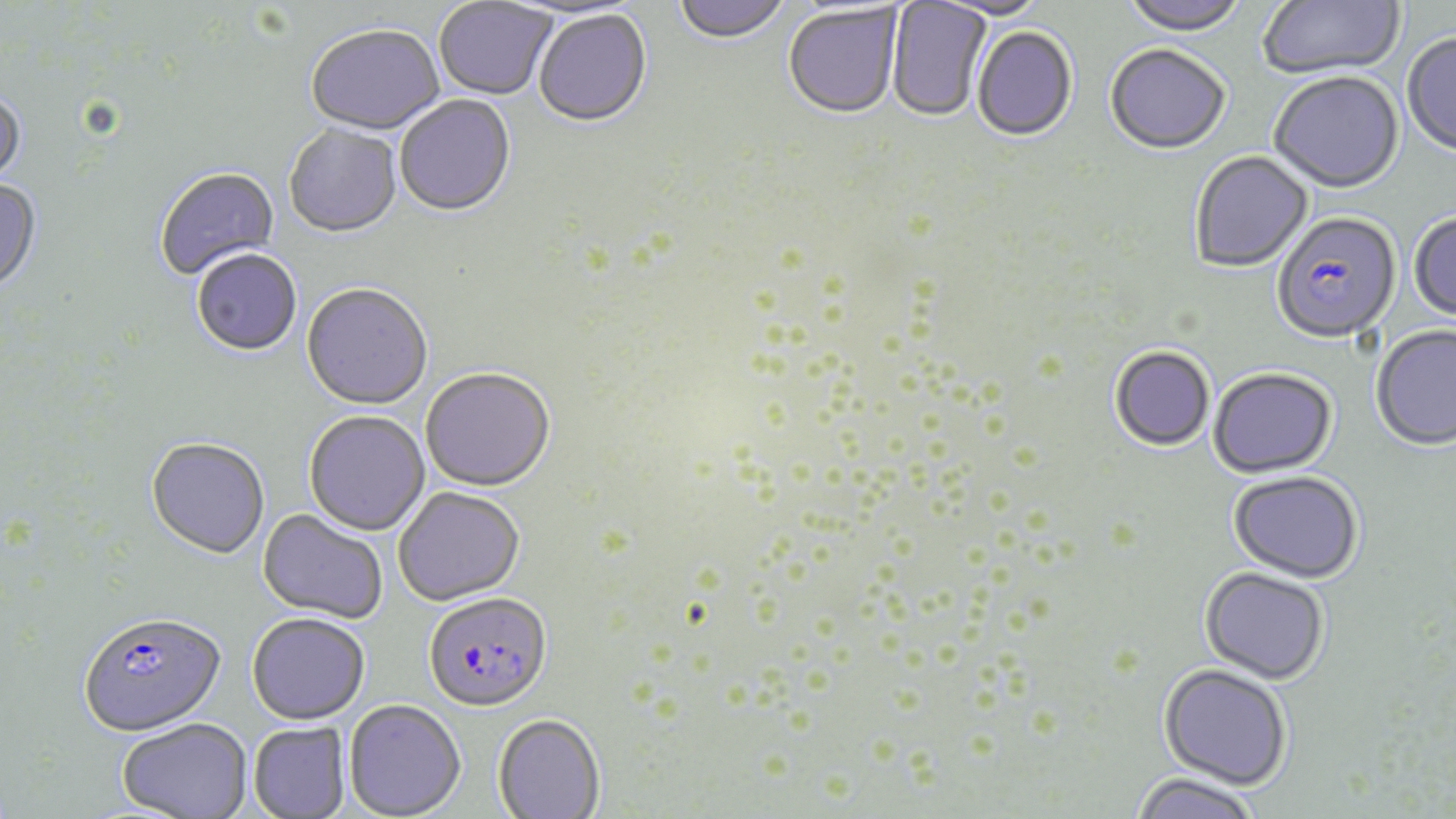 Approximate bounding boxes as (x1,y1)-(x2,y2) corner pairs in pixels. Uninfected red blood cell locations: (434,0)-(557,101), (673,0)-(792,46), (932,0)-(1052,22), (1120,0)-(1248,38), (1258,0)-(1406,82), (887,1)-(992,124), (782,5)-(903,121), (533,11)-(652,129), (306,26)-(445,138), (972,27)-(1078,144), (1402,34)-(1456,158), (1104,46)-(1231,157), (1268,74)-(1405,196), (0,91)-(27,193), (395,96)-(516,219), (283,125)-(402,239), (1190,152)-(1313,273), (154,168)-(280,282), (0,179)-(42,299), (1409,214)-(1456,324), (192,251)-(302,358), (301,284)-(434,412), (1371,326)-(1456,454), (1109,348)-(1215,453), (420,368)-(556,493), (1208,370)-(1337,480), (303,411)-(430,536), (146,438)-(270,561), (1228,472)-(1364,586), (393,486)-(525,607), (257,508)-(389,624), (1199,569)-(1329,686), (247,613)-(370,724), (1158,665)-(1291,792), (344,699)-(466,818), (493,714)-(605,818), (117,718)-(253,819), (249,722)-(351,819), (1128,775)-(1263,819). Plasmodium falciparum-infected red blood cell locations: (1271,214)-(1401,346), (423,592)-(552,712), (78,612)-(226,736). Slide-level diagnosis: Plasmodium falciparum. Thin blood film. Optical microscopy. Single field of view. May-Grünwald-Giemsa-stained preparation. Image is 1456×819 pixels. 1000x magnification.